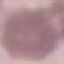

result = no malaria parasites detected
capture = smartphone camera at the microscope eyepiece
image type = cell patch, automatically extracted from a larger field of view and resized to 64 × 64 pixels
preparation = thin blood smear
stain = Giemsa